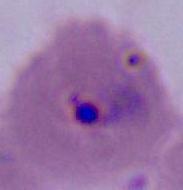
Summary:
  - Magnification: 400x or 1000x
  - Identification: Plasmodium
  - Modality: micrograph